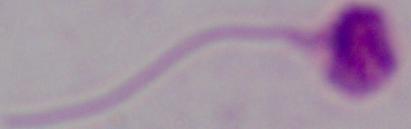

magnification: 1000x
modality: micrograph
identification: Leishmania